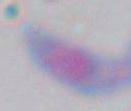 1000x magnification. Micrograph. Toxoplasma gondii is seen.